Give the position of every Plasmodium parasite and every leukocyte.
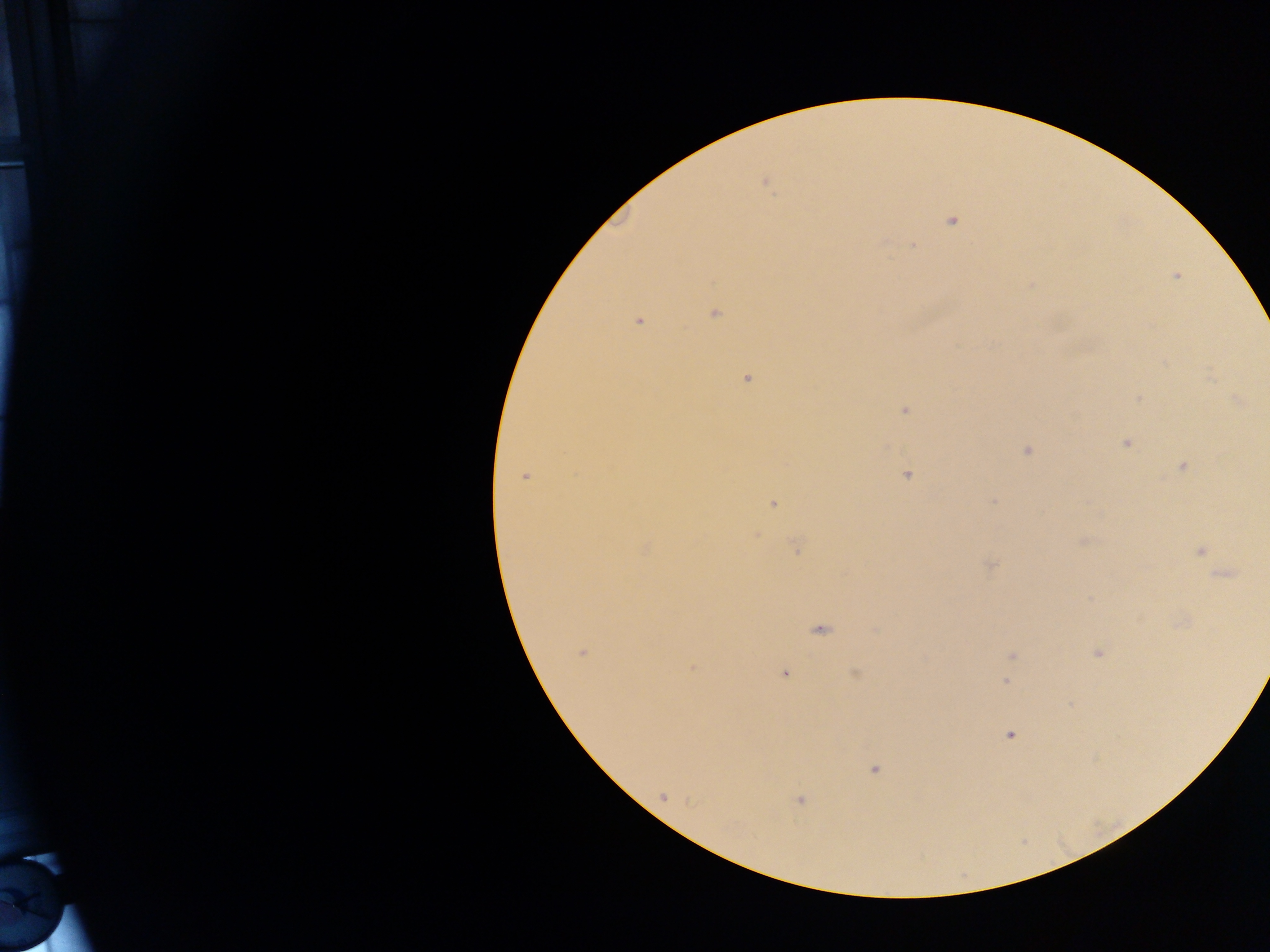

Approximate centers as (x, y) in pixels.
Plasmodium parasites: (764, 182), (951, 221), (913, 245), (1176, 276), (715, 314), (639, 321), (747, 379), (1138, 397), (1238, 401), (904, 411), (1125, 443), (1026, 451), (1182, 467), (907, 475), (525, 477), (993, 501), (773, 504), (756, 534), (1084, 540), (645, 547), (796, 547), (1201, 551), (990, 565), (1224, 575), (820, 630), (582, 652), (1098, 654), (1012, 655), (692, 667), (784, 674), (856, 674), (1006, 681), (1010, 736), (874, 770), (663, 797), (799, 800).
No leukocytes observed.

Summary:
  - Image size: 1270×952 pixels
  - Field of view: single
  - Country: Ghana
  - Capture: mobile-phone photograph through a microscope
  - Preparation: thick blood film